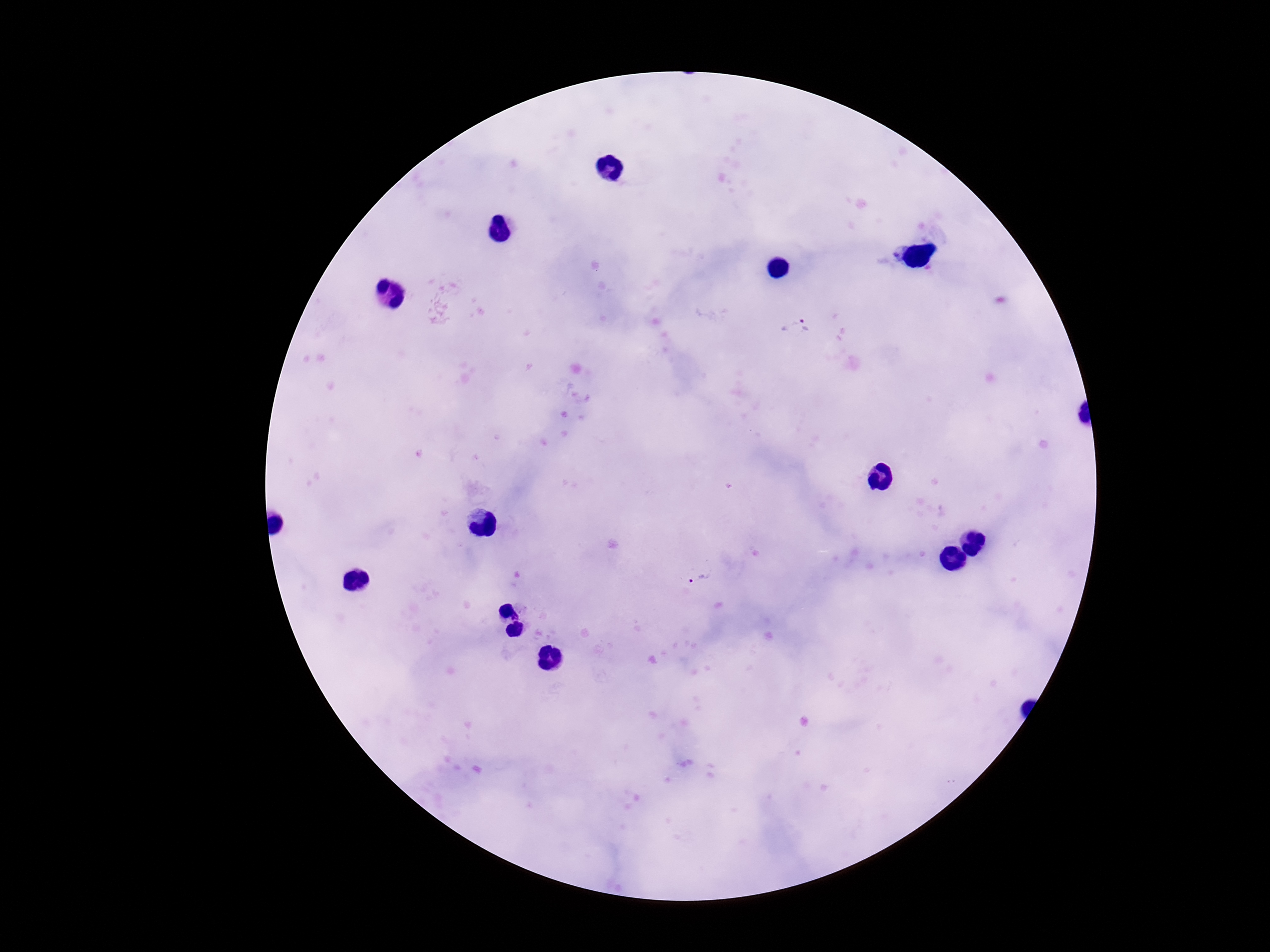

magnification = 100x
capture = smartphone camera through the microscope eyepiece
patient malaria status = positive
field of view = single
image size = 1270×952 pixels
Plasmodium parasite locations = approximate object centers, in pixels from the top-left corner: (x=797, y=327), (x=699, y=579)
stain = Giemsa
preparation = thick peripheral-blood smear